Locate every Babesia divergens-infected red blood cell.
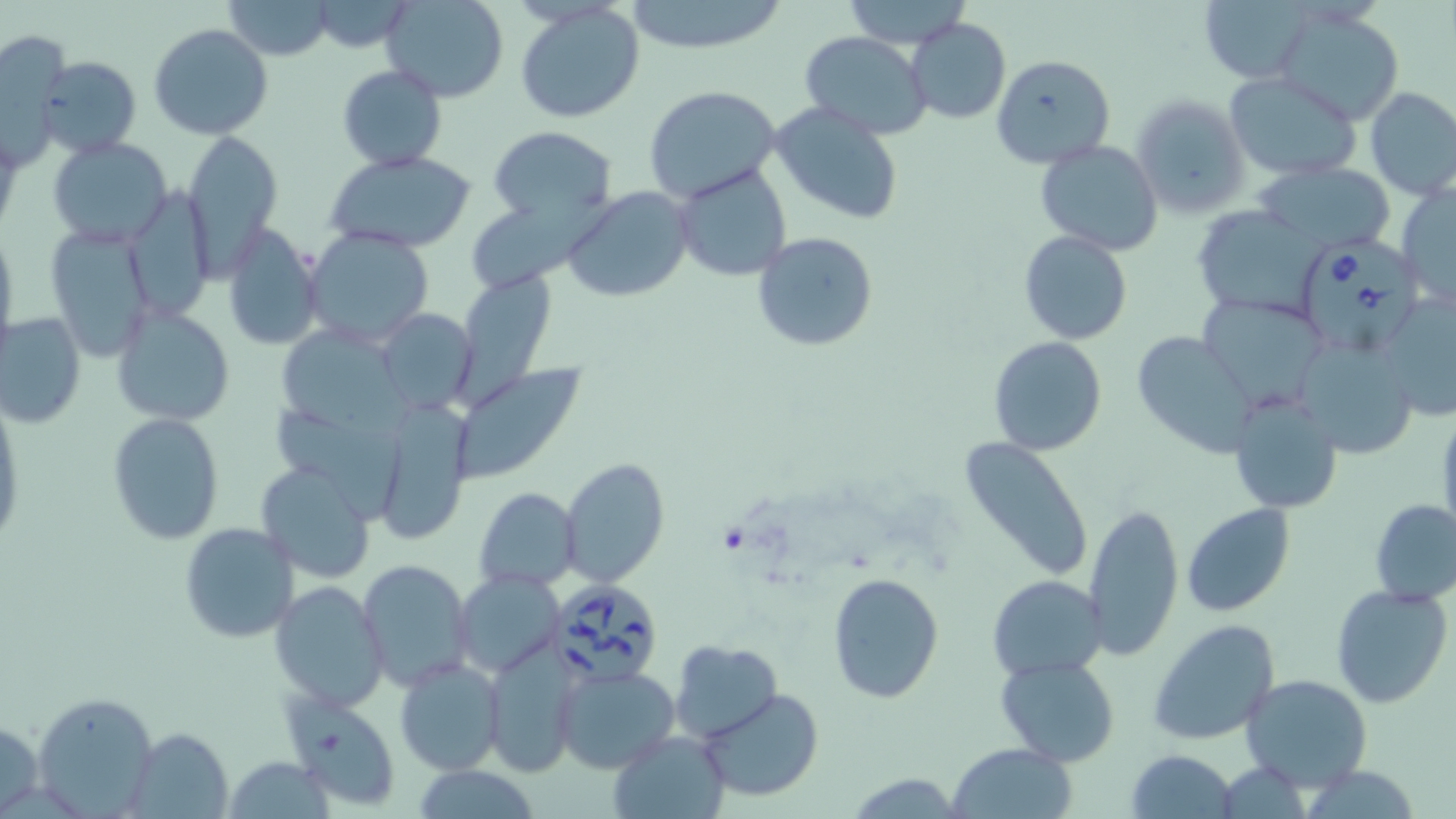
Approximate bounding boxes as [x1, y1, x2, y2] in pixels.
Babesia divergens-infected red blood cells: [1296, 232, 1436, 360], [553, 583, 662, 686].

slide_level_diagnosis: Babesia divergens
platelet_locations: 'approximate bounding boxes as [x1, y1, x2, y2] in pixels: [717, 525, 747, 553]'
magnification: 1000x
modality: optical microscopy
uninfected_red_blood_cell_locations: 'approximate bounding boxes as [x1, y1, x2, y2] in pixels: [225, 0, 331, 60], [382, 0, 509, 102], [841, 0, 971, 48], [623, 1, 789, 55], [1195, 1, 1314, 82], [309, 4, 414, 51], [514, 4, 645, 124], [1274, 10, 1405, 125], [906, 18, 1011, 123], [149, 23, 274, 141], [3, 26, 68, 157], [799, 31, 932, 138], [991, 54, 1115, 169], [35, 55, 140, 160], [337, 64, 446, 171], [1226, 73, 1363, 180], [645, 85, 783, 207], [1364, 86, 1456, 199], [1131, 93, 1250, 219], [769, 102, 906, 226], [488, 125, 617, 225], [182, 132, 283, 270], [47, 138, 173, 247], [1034, 140, 1165, 256], [325, 149, 479, 253], [1259, 162, 1396, 253], [673, 163, 792, 281], [1396, 181, 1455, 311], [562, 187, 694, 301], [134, 193, 213, 324], [467, 199, 626, 287], [1192, 205, 1328, 321], [42, 222, 156, 360], [0, 224, 18, 352], [222, 226, 324, 351], [304, 227, 435, 346], [754, 231, 877, 351], [1018, 231, 1135, 346], [460, 277, 562, 411], [1378, 289, 1456, 419], [1200, 294, 1329, 410], [111, 305, 234, 425], [375, 308, 475, 413], [0, 310, 85, 429], [279, 319, 412, 449], [1130, 331, 1259, 458], [989, 337, 1108, 456], [1296, 337, 1418, 459], [449, 365, 586, 483], [267, 393, 408, 521], [1230, 393, 1343, 514], [373, 395, 477, 541], [1434, 406, 1456, 544], [107, 413, 225, 544], [959, 438, 1095, 582], [560, 458, 669, 588], [255, 462, 377, 583], [475, 487, 579, 592], [1369, 498, 1456, 606], [1084, 501, 1184, 660], [1181, 503, 1295, 616], [179, 522, 301, 644], [356, 560, 474, 693], [454, 569, 565, 679], [828, 572, 943, 701], [988, 574, 1109, 679], [269, 581, 390, 711], [1330, 584, 1452, 709], [1148, 618, 1281, 745], [668, 640, 781, 741], [483, 642, 583, 777], [394, 655, 505, 776], [996, 656, 1120, 768], [552, 665, 679, 773], [1240, 674, 1371, 792], [283, 687, 402, 809], [700, 688, 822, 802], [32, 689, 160, 818], [1, 717, 45, 815], [126, 726, 234, 818], [608, 729, 730, 819], [947, 742, 1077, 819], [1126, 749, 1238, 819], [222, 758, 330, 818]'
image_size: 1456×819 pixels
preparation: thin blood film
field_of_view: single
stain: May-Grünwald-Giemsa